Classify this cell by malaria status.
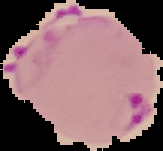

It is parasitized.

{
  "preparation": "thin blood film",
  "image_size": "163×151 pixels",
  "image_type": "segmented cell region on a black background"
}